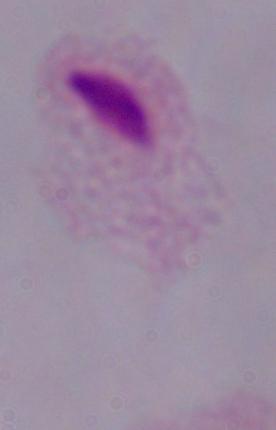

{
  "modality": "micrograph",
  "magnification": "1000x",
  "identification": "trichomonad"
}